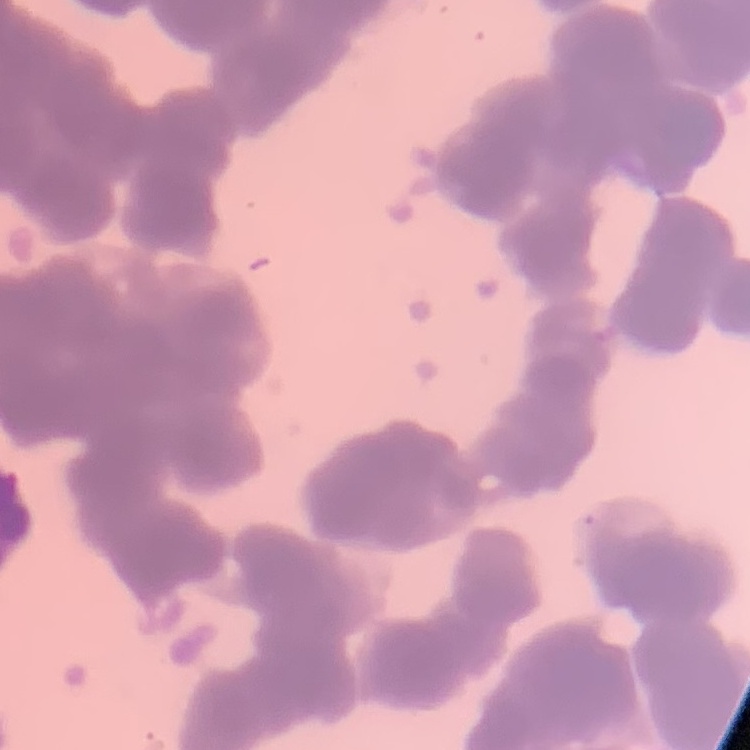
The erythrocytes show rouleaux formation. Thin peripheral smear. Field's or Giemsa stain. One tile cut from a larger photomicrograph.